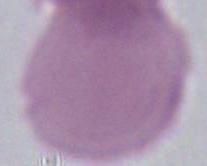
magnification: 1000x
identification: red blood cell
modality: micrograph